Report the malaria status of this cell.
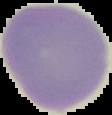

Uninfected.

Image is 112×115 pixels. Segmented cell region on a black background. From a thin blood smear.